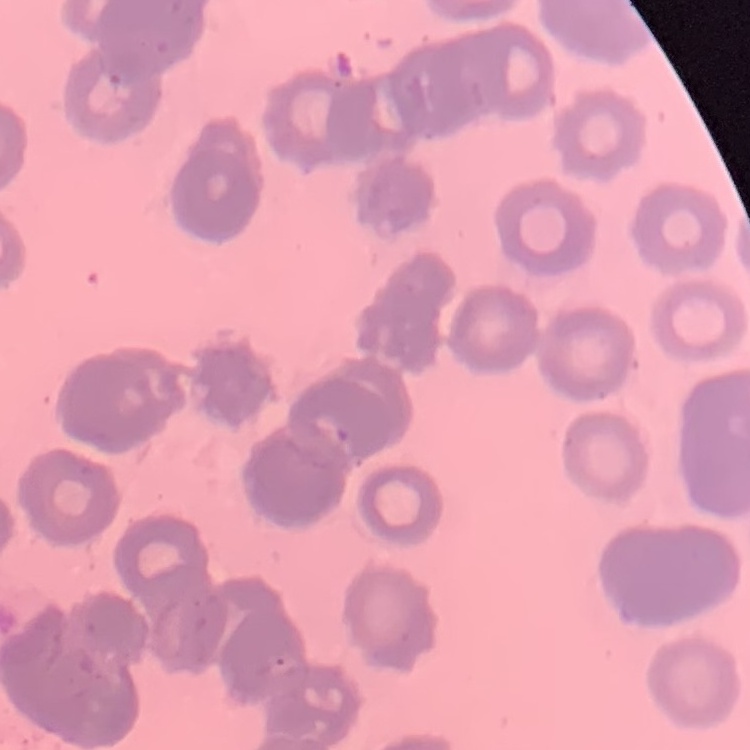
red blood cell morphology = rouleaux formation
preparation = thin blood smear
stain = Field's or Giemsa
image type = square crop of a larger photomicrograph